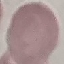 Result: no malaria parasites seen. Acquired by smartphone through the microscope eyepiece. Giemsa stain. Automatically extracted cell patch, resized to 64 × 64 pixels. Thin blood smear.